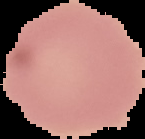
malaria status = uninfected
preparation = thin blood film
image type = segmented cell region on a black background
image size = 145×139 pixels